Locate every Plasmodium parasite and every leukocyte.
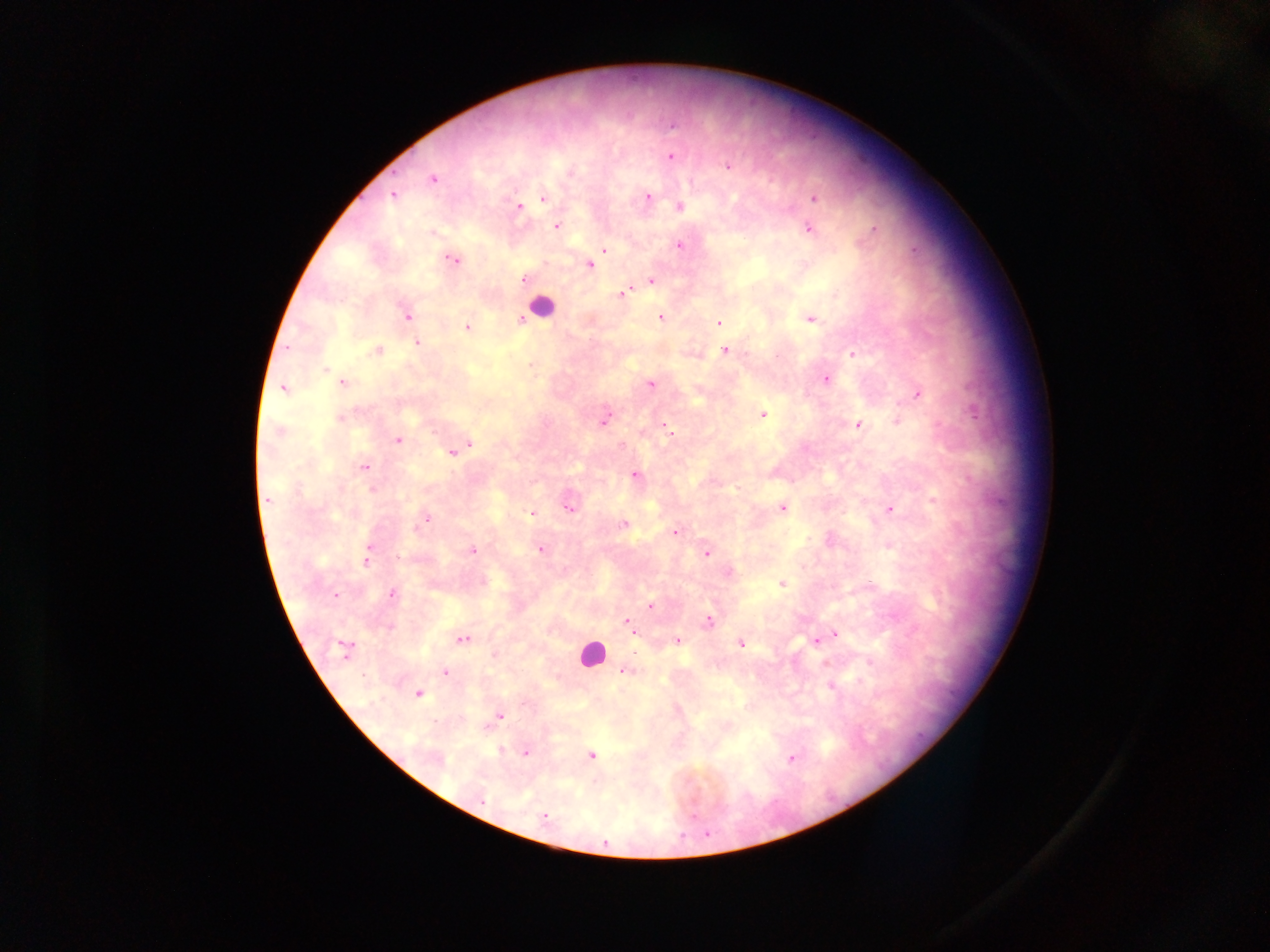

Approximate centers as {x, y} in pixels.
Plasmodium parasites: {671, 125}, {670, 156}, {728, 166}, {433, 178}, {393, 194}, {647, 196}, {814, 198}, {542, 199}, {518, 207}, {679, 207}, {556, 225}, {808, 228}, {874, 229}, {433, 233}, {680, 244}, {603, 249}, {452, 258}, {589, 265}, {524, 280}, {652, 280}, {626, 291}, {406, 315}, {660, 317}, {809, 318}, {521, 319}, {719, 323}, {466, 327}, {416, 343}, {377, 350}, {725, 350}, {853, 354}, {327, 369}, {826, 378}, {342, 382}, {650, 384}, {284, 387}, {916, 393}, {763, 415}, {340, 418}, {603, 420}, {896, 421}, {662, 424}, {858, 424}, {278, 431}, {397, 439}, {454, 450}, {363, 467}, {634, 474}, {268, 499}, {568, 505}, {782, 507}, {889, 510}, {532, 514}, {423, 520}, {622, 524}, {674, 532}, {888, 545}, {540, 549}, {471, 550}, {706, 553}, {367, 557}, {729, 573}, {481, 581}, {781, 583}, {392, 594}, {650, 605}, {708, 622}, {627, 623}, {835, 633}, {462, 639}, {817, 639}, {677, 641}, {741, 643}, {343, 649}, {494, 654}, {627, 669}, {445, 672}, {831, 686}, {418, 693}, {499, 715}, {501, 750}, {524, 752}, {591, 756}, {791, 757}, {543, 816}.
Leukocytes: {540, 305}, {591, 654}.

capture = mobile-phone photograph through a microscope
country = Ghana
image size = 1270×952 pixels
preparation = thick blood film
field of view = single